Outline each blood parasite and name the species.
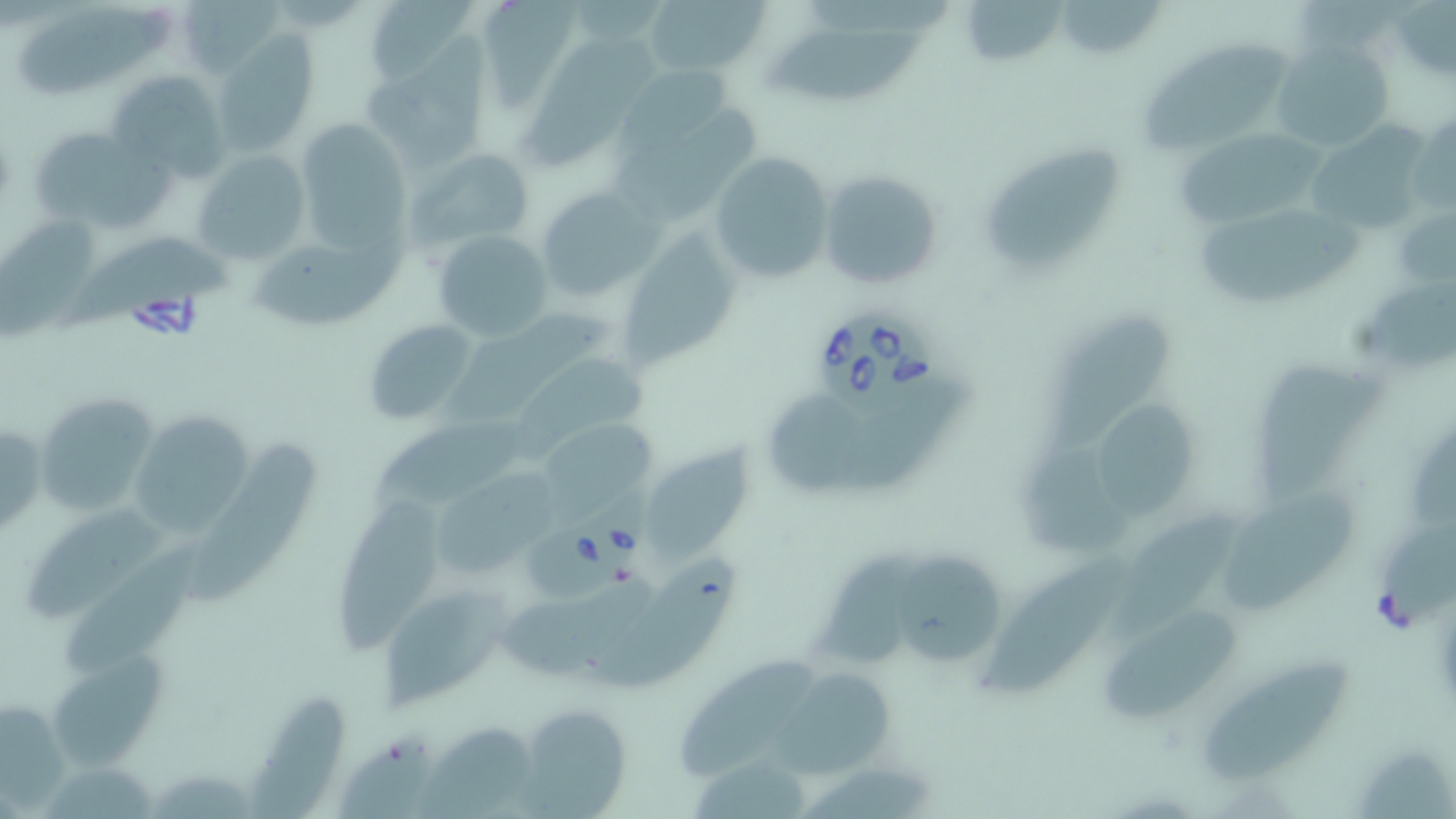
Approximate bounding boxes as named x1/y1/x2/y2 corners in pixels.
Babesia divergens-infected red blood cells: (x1=820, y1=310, x2=939, y2=413), (x1=534, y1=486, x2=662, y2=599).
No Plasmodium falciparum, Plasmodium ovale, Plasmodium malariae, Plasmodium vivax, or Trypanosoma brucei observed.

{
  "slide_level_diagnosis": "Babesia divergens",
  "stain": "May-Grünwald-Giemsa",
  "preparation": "thin blood smear",
  "image_size": "1456×819 pixels",
  "field_of_view": "single",
  "modality": "optical microscopy",
  "magnification": "1000x",
  "uninfected_red_blood_cell_locations": "approximate bounding boxes as named x1/y1/x2/y2 corners in pixels: (x1=367, y1=0, x2=477, y2=91), (x1=642, y1=0, x2=769, y2=82), (x1=967, y1=0, x2=1067, y2=66), (x1=1062, y1=0, x2=1170, y2=59), (x1=185, y1=2, x2=285, y2=76), (x1=806, y1=2, x2=955, y2=42), (x1=485, y1=3, x2=587, y2=103), (x1=21, y1=4, x2=169, y2=103), (x1=770, y1=23, x2=931, y2=103), (x1=362, y1=27, x2=498, y2=176), (x1=212, y1=33, x2=317, y2=157), (x1=520, y1=36, x2=660, y2=170), (x1=1144, y1=39, x2=1289, y2=160), (x1=1272, y1=42, x2=1393, y2=153), (x1=620, y1=59, x2=738, y2=158), (x1=109, y1=69, x2=231, y2=184), (x1=613, y1=111, x2=762, y2=225), (x1=1308, y1=111, x2=1435, y2=234), (x1=1411, y1=112, x2=1455, y2=216), (x1=295, y1=118, x2=419, y2=259), (x1=1174, y1=126, x2=1327, y2=222), (x1=37, y1=133, x2=188, y2=235), (x1=983, y1=141, x2=1125, y2=273), (x1=405, y1=148, x2=535, y2=253), (x1=190, y1=149, x2=310, y2=268), (x1=707, y1=151, x2=837, y2=285), (x1=818, y1=169, x2=944, y2=293), (x1=536, y1=186, x2=660, y2=299), (x1=1198, y1=202, x2=1366, y2=307), (x1=1393, y1=206, x2=1453, y2=291), (x1=0, y1=214, x2=109, y2=339), (x1=620, y1=219, x2=744, y2=369), (x1=430, y1=228, x2=555, y2=342), (x1=247, y1=235, x2=423, y2=327), (x1=65, y1=239, x2=241, y2=336), (x1=1360, y1=284, x2=1455, y2=371), (x1=446, y1=311, x2=622, y2=421), (x1=1044, y1=312, x2=1172, y2=461), (x1=363, y1=319, x2=480, y2=426), (x1=518, y1=351, x2=655, y2=454), (x1=1256, y1=357, x2=1387, y2=503), (x1=830, y1=377, x2=982, y2=491), (x1=768, y1=393, x2=860, y2=490), (x1=37, y1=395, x2=154, y2=513), (x1=1097, y1=403, x2=1199, y2=521), (x1=365, y1=412, x2=546, y2=512), (x1=133, y1=414, x2=252, y2=531), (x1=542, y1=423, x2=652, y2=514), (x1=1411, y1=432, x2=1456, y2=534), (x1=650, y1=435, x2=767, y2=564), (x1=196, y1=436, x2=322, y2=603), (x1=1017, y1=452, x2=1139, y2=552), (x1=437, y1=463, x2=568, y2=579), (x1=1223, y1=487, x2=1358, y2=618), (x1=338, y1=496, x2=445, y2=665), (x1=1111, y1=498, x2=1240, y2=646), (x1=29, y1=503, x2=173, y2=624), (x1=1382, y1=524, x2=1456, y2=626), (x1=64, y1=542, x2=210, y2=678), (x1=894, y1=542, x2=1015, y2=667), (x1=822, y1=545, x2=932, y2=671), (x1=984, y1=548, x2=1122, y2=699), (x1=596, y1=557, x2=742, y2=689), (x1=502, y1=576, x2=654, y2=675), (x1=380, y1=585, x2=517, y2=712), (x1=1103, y1=604, x2=1237, y2=721), (x1=54, y1=652, x2=177, y2=772), (x1=672, y1=653, x2=817, y2=787), (x1=1205, y1=654, x2=1354, y2=784), (x1=780, y1=671, x2=899, y2=776), (x1=246, y1=688, x2=343, y2=819), (x1=2, y1=701, x2=73, y2=819), (x1=517, y1=704, x2=630, y2=815), (x1=418, y1=727, x2=553, y2=819), (x1=338, y1=729, x2=442, y2=819), (x1=1359, y1=738, x2=1456, y2=819), (x1=693, y1=757, x2=824, y2=819), (x1=44, y1=764, x2=160, y2=819), (x1=800, y1=766, x2=950, y2=819), (x1=150, y1=768, x2=270, y2=819)"
}